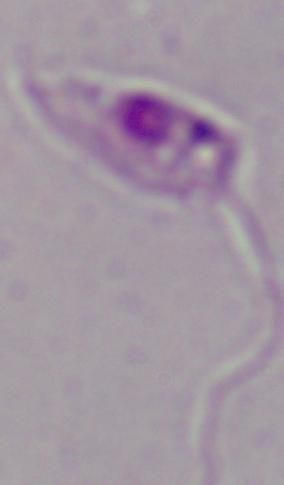

identification: Leishmania
modality: micrograph
magnification: 1000x